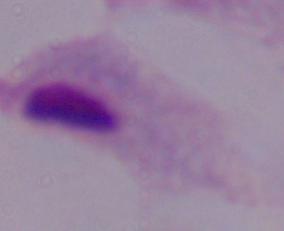

Summary:
  - Magnification: 1000x
  - Modality: photomicrograph
  - Identification: trichomonad